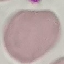
Summary:
  - Malaria status: uninfected
  - Image type: automatically extracted cell patch, resized to 64 × 64 pixels
  - Stain: Giemsa
  - Capture: smartphone through the microscope eyepiece
  - Preparation: thin blood smear